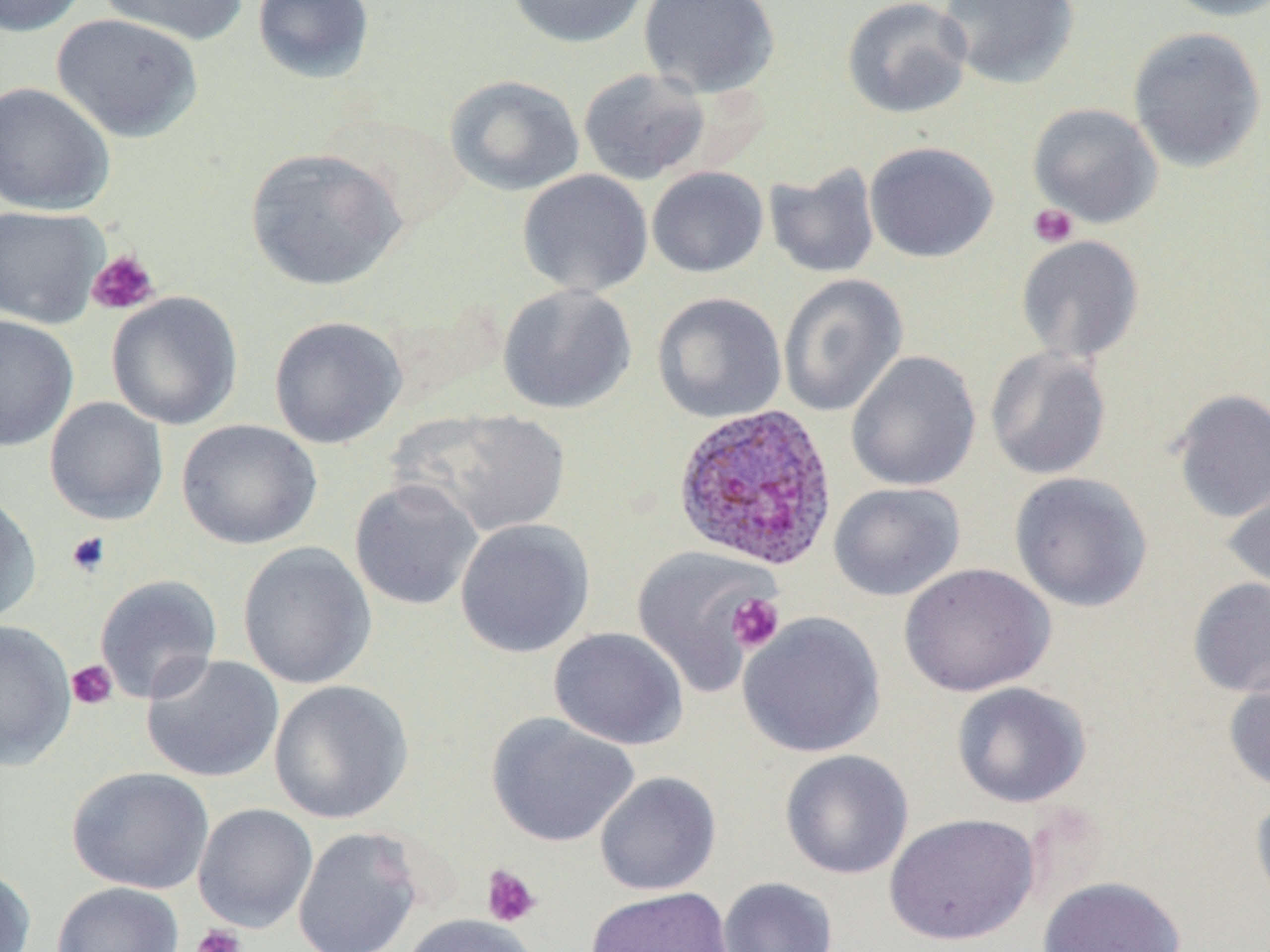

slide-level diagnosis = Plasmodium ovale
field of view = one of a larger specimen
Plasmodium ovale-infected red blood cell locations = approximate bounding boxes as [x1, y1, x2, y2] in pixels: [671, 403, 839, 572]
stain = May-Grünwald-Giemsa
image size = 1270×952 pixels
platelet locations = approximate bounding boxes as [x1, y1, x2, y2] in pixels: [1028, 203, 1079, 248], [88, 249, 160, 315], [65, 531, 111, 578], [726, 593, 784, 652], [66, 660, 118, 709], [481, 865, 541, 928], [192, 924, 246, 952]
magnification = 1000x
preparation = thin blood film
modality = light microscopy
uninfected red blood cell locations = approximate bounding boxes as [x1, y1, x2, y2] in pixels: [0, 0, 88, 37], [97, 0, 248, 46], [252, 0, 375, 83], [505, 0, 650, 48], [637, 0, 781, 99], [842, 0, 973, 120], [938, 0, 1080, 89], [1160, 0, 1270, 22], [51, 13, 204, 144], [1127, 26, 1267, 172], [577, 67, 710, 185], [444, 74, 584, 197], [0, 81, 116, 216], [1027, 102, 1163, 227], [864, 141, 999, 263], [244, 147, 407, 291], [764, 163, 881, 279], [647, 166, 769, 278], [517, 169, 653, 298], [0, 204, 108, 329], [1015, 234, 1145, 364], [777, 273, 908, 417], [497, 283, 637, 414], [106, 291, 243, 430], [652, 292, 787, 424], [0, 314, 79, 452], [269, 315, 407, 449], [984, 347, 1112, 480], [845, 350, 982, 492], [1169, 388, 1270, 524], [44, 397, 169, 525], [397, 407, 572, 539], [176, 419, 323, 550], [1009, 472, 1153, 612], [1223, 477, 1270, 598], [348, 478, 484, 611], [827, 482, 966, 601], [0, 490, 42, 626], [455, 518, 596, 658], [237, 541, 377, 689], [631, 545, 778, 696], [898, 562, 1055, 697], [94, 574, 222, 704], [1187, 576, 1270, 698], [738, 611, 886, 758], [0, 619, 77, 771], [548, 627, 688, 750], [141, 653, 284, 783], [1222, 666, 1270, 794], [269, 680, 413, 824], [951, 681, 1091, 809], [486, 713, 639, 848], [780, 749, 914, 879], [66, 766, 214, 895], [594, 771, 722, 896], [1250, 787, 1270, 918], [193, 803, 318, 933], [884, 812, 1039, 946], [292, 826, 424, 952], [0, 865, 36, 952], [1038, 875, 1186, 952], [717, 876, 838, 952], [51, 882, 184, 952], [585, 886, 734, 951], [401, 913, 538, 952]